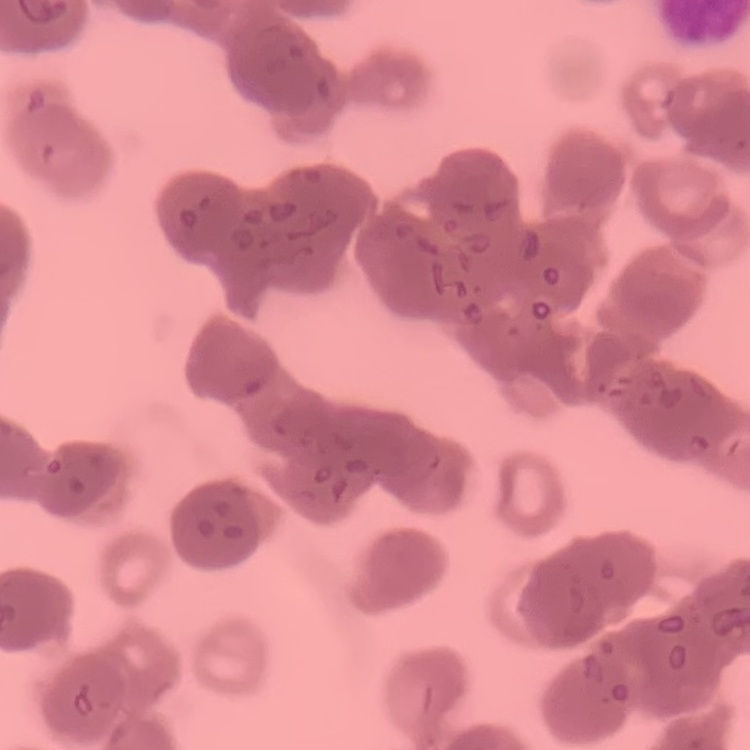
The erythrocytes show rouleaux formation. Stained with either Field's or Giemsa. Square crop of a larger photomicrograph. Thin blood film.